Outline each blood parasite and name the species.
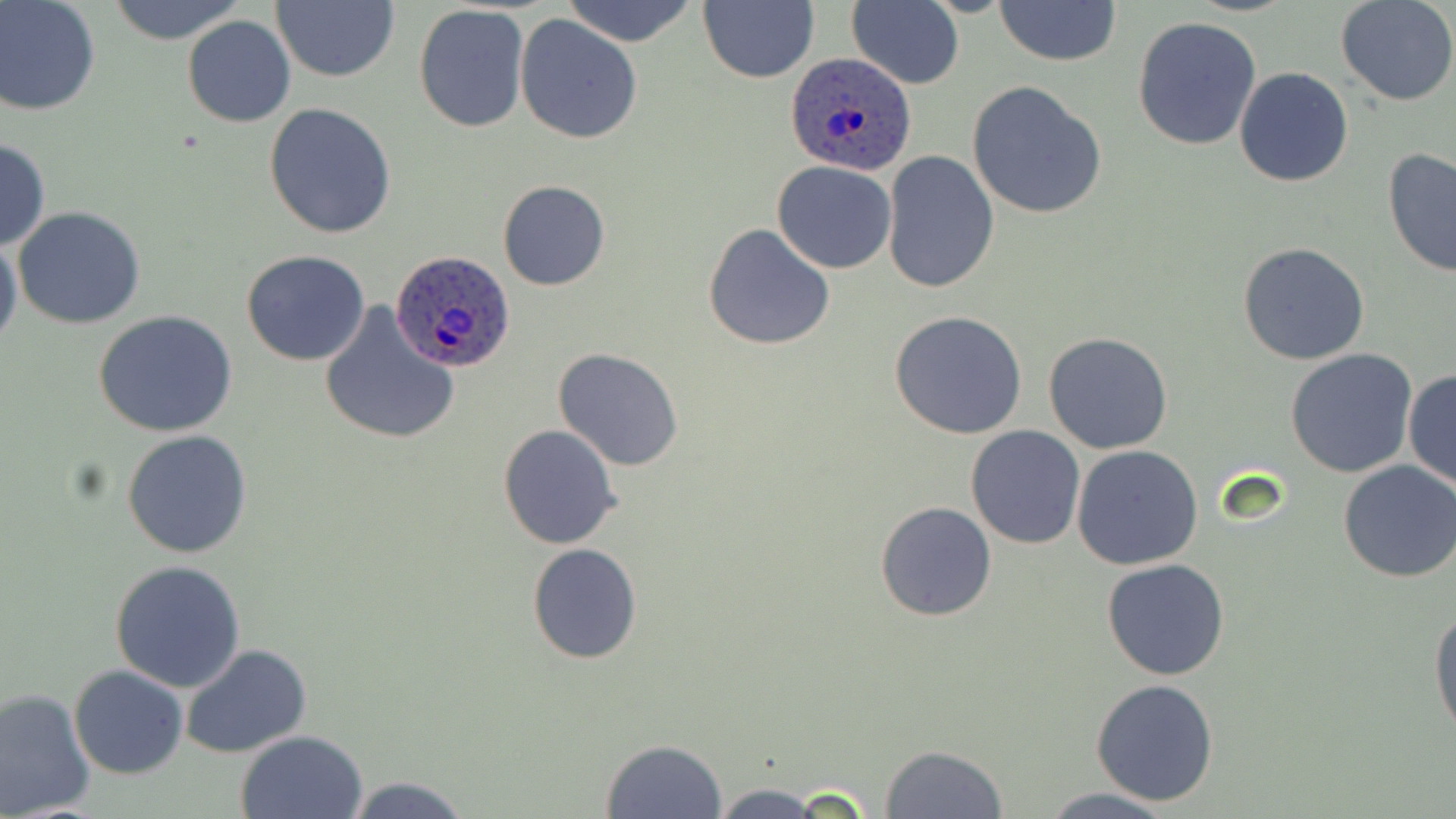

Approximate bounding boxes as named x1/y1/x2/y2 corners in pixels.
Plasmodium ovale-infected red blood cells: (x1=784, y1=53, x2=915, y2=173), (x1=391, y1=251, x2=517, y2=374).
No Plasmodium falciparum, Plasmodium malariae, Plasmodium vivax, Babesia divergens, or Trypanosoma brucei observed.

Uninfected red blood cell locations: (x1=273, y1=0, x2=401, y2=83), (x1=560, y1=0, x2=700, y2=47), (x1=698, y1=0, x2=818, y2=84), (x1=846, y1=0, x2=964, y2=90), (x1=995, y1=0, x2=1121, y2=66), (x1=1335, y1=0, x2=1456, y2=106), (x1=0, y1=1, x2=101, y2=117), (x1=103, y1=1, x2=249, y2=44), (x1=412, y1=4, x2=529, y2=135), (x1=514, y1=12, x2=643, y2=144), (x1=182, y1=15, x2=296, y2=127), (x1=1132, y1=16, x2=1263, y2=151), (x1=1233, y1=66, x2=1356, y2=186), (x1=967, y1=80, x2=1109, y2=219), (x1=263, y1=102, x2=397, y2=240), (x1=0, y1=138, x2=50, y2=251), (x1=1381, y1=148, x2=1456, y2=279), (x1=881, y1=150, x2=999, y2=294), (x1=771, y1=161, x2=897, y2=273), (x1=496, y1=180, x2=611, y2=291), (x1=12, y1=206, x2=146, y2=331), (x1=703, y1=222, x2=837, y2=352), (x1=0, y1=235, x2=23, y2=355), (x1=1237, y1=242, x2=1370, y2=366), (x1=242, y1=250, x2=370, y2=366), (x1=316, y1=301, x2=461, y2=448), (x1=93, y1=310, x2=237, y2=437), (x1=888, y1=311, x2=1029, y2=440), (x1=1043, y1=332, x2=1174, y2=455), (x1=552, y1=347, x2=685, y2=471), (x1=1285, y1=348, x2=1419, y2=479), (x1=1403, y1=368, x2=1456, y2=492), (x1=498, y1=424, x2=622, y2=550), (x1=965, y1=426, x2=1086, y2=550), (x1=122, y1=429, x2=253, y2=560), (x1=1071, y1=445, x2=1203, y2=569), (x1=1338, y1=459, x2=1456, y2=583), (x1=877, y1=501, x2=998, y2=621), (x1=528, y1=543, x2=642, y2=664), (x1=1101, y1=558, x2=1231, y2=681), (x1=110, y1=559, x2=245, y2=692), (x1=1427, y1=603, x2=1456, y2=741), (x1=180, y1=643, x2=312, y2=760), (x1=69, y1=665, x2=190, y2=779), (x1=1090, y1=678, x2=1220, y2=806), (x1=0, y1=687, x2=97, y2=819), (x1=235, y1=730, x2=368, y2=818), (x1=600, y1=739, x2=728, y2=818), (x1=878, y1=745, x2=1009, y2=819), (x1=343, y1=776, x2=472, y2=818), (x1=703, y1=782, x2=834, y2=819), (x1=1035, y1=788, x2=1184, y2=818). Slide-level diagnosis: Plasmodium ovale. 1000x magnification. Image is 1456×819 pixels. Light microscopy. One field of a larger specimen. Thin blood film. May-Grünwald-Giemsa stain.